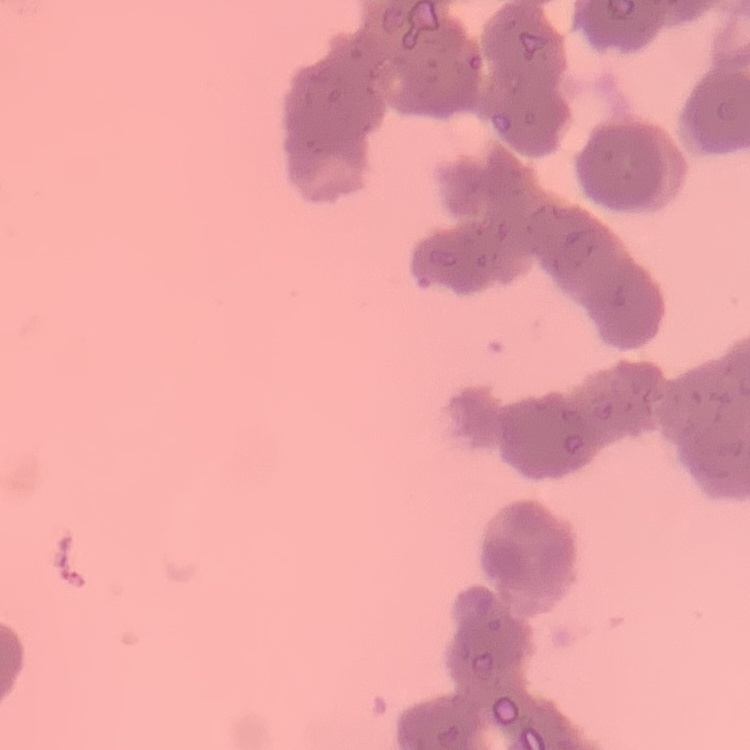 The erythrocytes exhibit rouleaux formation. Stained with either Field's or Giemsa. Thin peripheral smear. Square crop of a larger photomicrograph.